State which cell type is depicted.
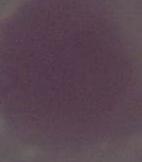
An erythrocyte.

Summary:
  - Magnification: 1000x
  - Modality: micrograph